State which parasite is depicted.
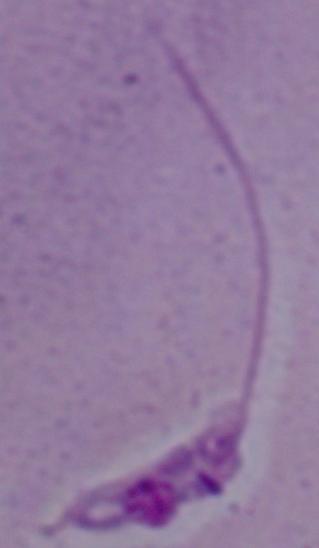
Leishmania.

modality = micrograph
magnification = 1000x